Assess this cell for malaria.
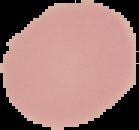
Uninfected.

Image is 139×130 pixels. The area outside the segmented cell region is set to black. From a thin blood smear.